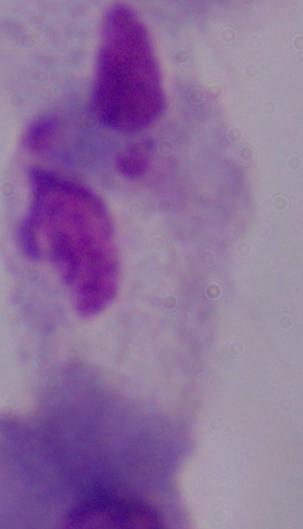

modality = micrograph
identification = trichomonad
magnification = 1000x